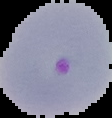

From a thin blood smear. Segmented cell region on a black background. Image is 112×118 pixels. Malaria status: parasitized.